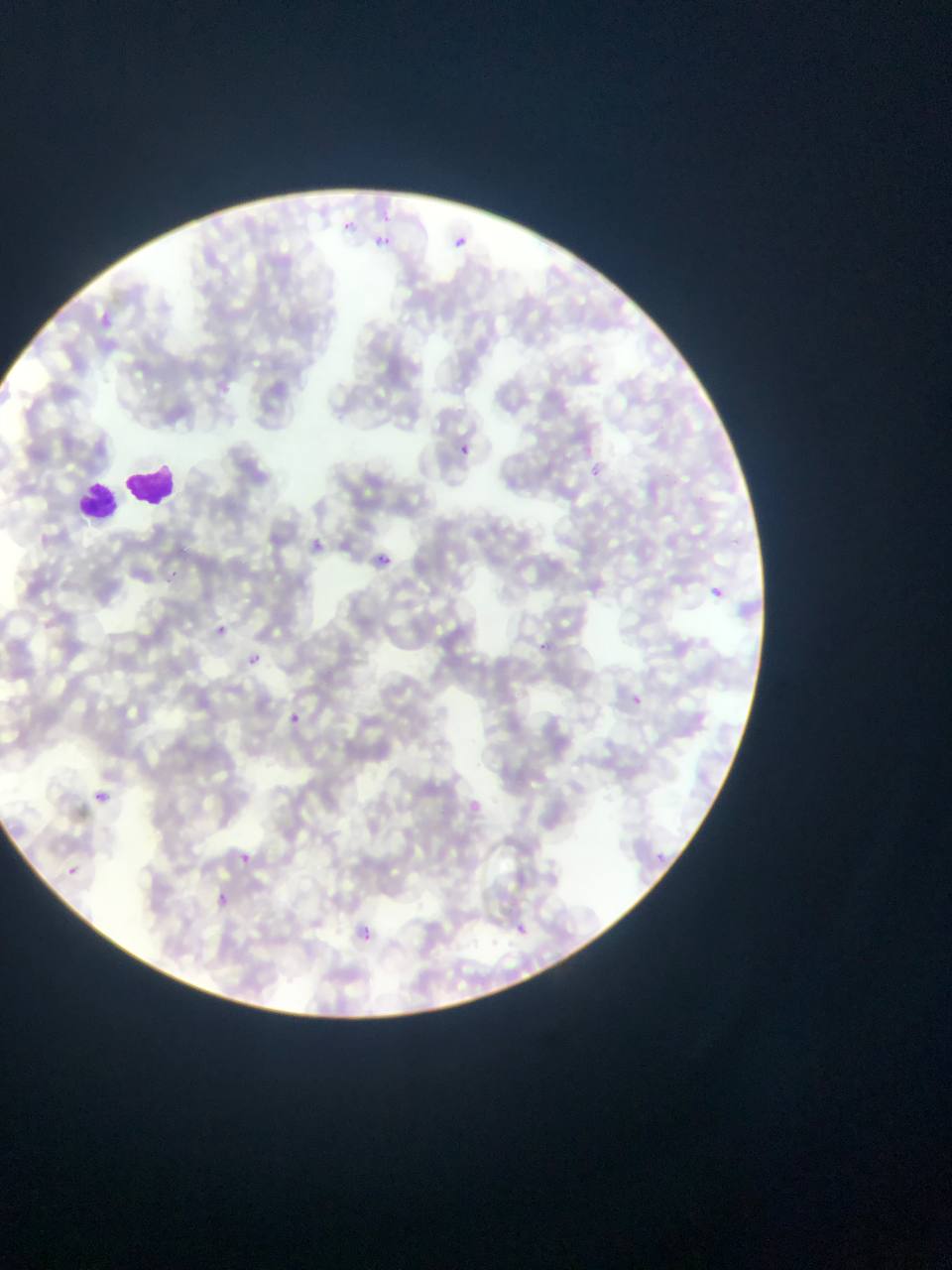
{
  "country": "Ghana",
  "preparation": "thin blood film",
  "capture": "mobile-phone photograph through a microscope",
  "malaria_parasite_locations": "approximate bounding boxes as {left, top, right, bottom} in pixels: {329, 218, 359, 235}, {374, 232, 392, 258}, {440, 233, 473, 254}, {93, 301, 128, 342}, {454, 441, 474, 460}, {302, 532, 357, 587}, {371, 553, 393, 572}, {163, 569, 180, 585}, {708, 584, 728, 601}, {532, 636, 556, 657}, {245, 652, 261, 667}, {624, 691, 646, 711}, {283, 709, 308, 731}, {92, 791, 108, 806}, {645, 846, 674, 871}, {230, 847, 259, 870}, {63, 864, 80, 879}, {210, 890, 234, 913}, {506, 918, 532, 940}, {348, 920, 381, 949}",
  "image_size": "952×1270 pixels",
  "leukocyte_locations": "approximate bounding boxes as {left, top, right, bottom} in pixels: {121, 459, 179, 511}, {85, 472, 178, 521}, {75, 476, 124, 524}",
  "field_of_view": "single"
}